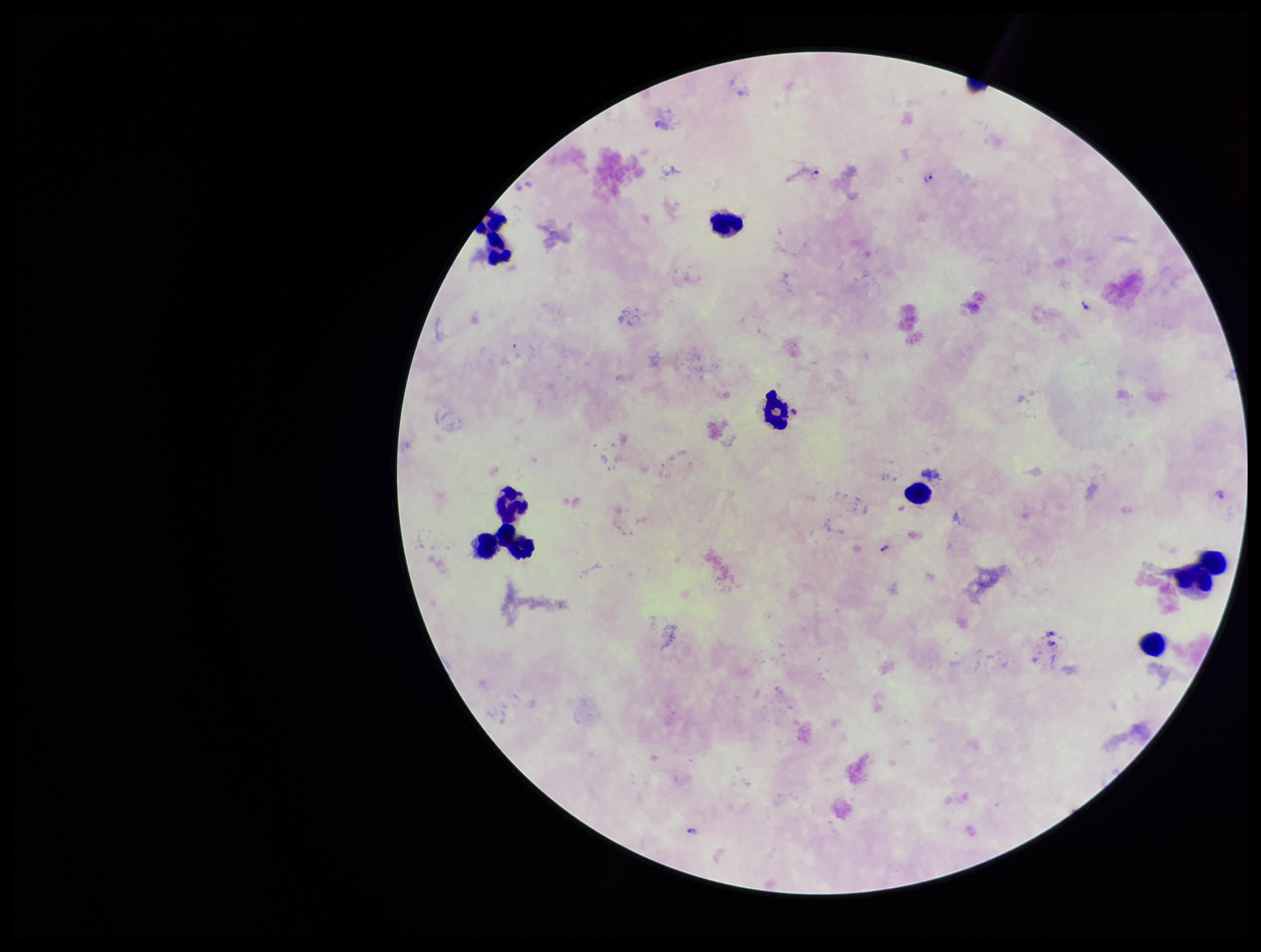

preparation = thick
image size = 1261×952 pixels
Plasmodium parasites = seen
leukocyte count = 9
capture = smartphone photograph through the microscope eyepiece
stain = Giemsa
field of view = single
parasite count = 7
species reported for this patient = Plasmodium falciparum
patient malaria status = infected